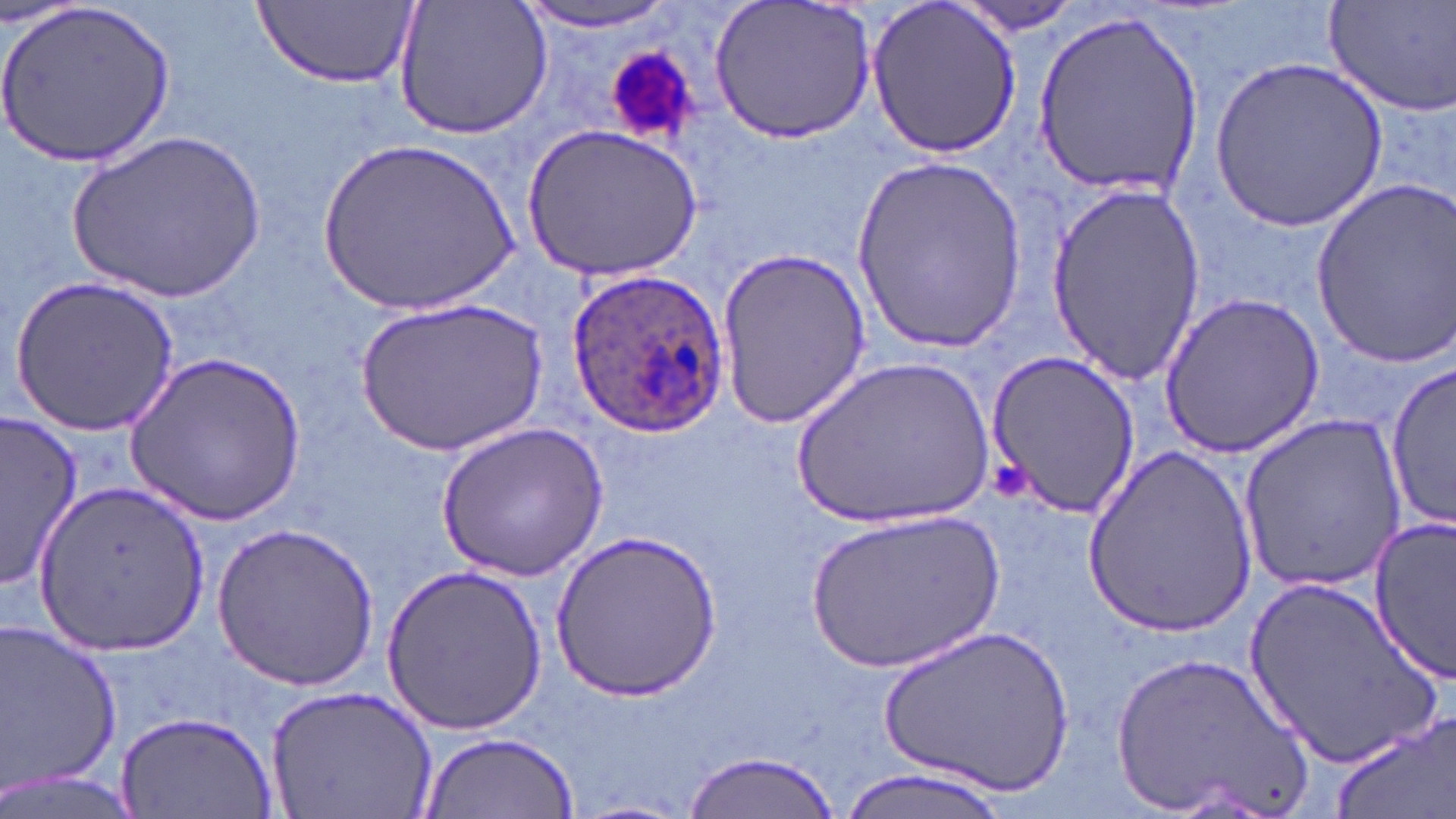

Approximate bounding boxes as (x1,y1)-(x2,y2) corner pairs in pixels. Uninfected red blood cell locations: (0,0)-(177,168), (392,0)-(553,142), (710,0)-(877,145), (866,0)-(1023,158), (1323,0)-(1456,119), (254,1)-(417,88), (514,1)-(685,36), (949,2)-(1087,38), (1029,9)-(1206,201), (1210,58)-(1391,229), (520,121)-(701,281), (70,129)-(263,302), (319,134)-(520,317), (848,155)-(1028,352), (1307,176)-(1456,371), (1043,181)-(1206,386), (716,247)-(872,429), (12,277)-(180,434), (1158,289)-(1325,460), (356,295)-(548,456), (127,348)-(304,526), (983,348)-(1140,522), (792,351)-(997,532), (1385,362)-(1454,528), (2,409)-(84,591), (1237,414)-(1407,593), (434,418)-(609,583), (1084,442)-(1258,635), (35,478)-(213,660), (803,508)-(1007,674), (1368,516)-(1453,684), (209,520)-(380,688), (553,529)-(721,701), (380,565)-(549,737), (1239,574)-(1445,769), (0,616)-(123,800), (885,625)-(1076,793), (1110,645)-(1319,819), (264,684)-(440,819), (116,707)-(277,817), (1327,711)-(1456,819), (419,729)-(580,818), (679,750)-(846,819), (833,765)-(1015,818), (0,766)-(139,819). Platelet locations: (603,43)-(703,141), (993,460)-(1029,500). Plasmodium ovale-infected red blood cell locations: (566,266)-(730,439). Slide-level diagnosis: Plasmodium ovale. 1000x magnification. Light microscopy. Image is 1456×819 pixels. Single field of view. Thin blood film. May-Grünwald-Giemsa-stained preparation.